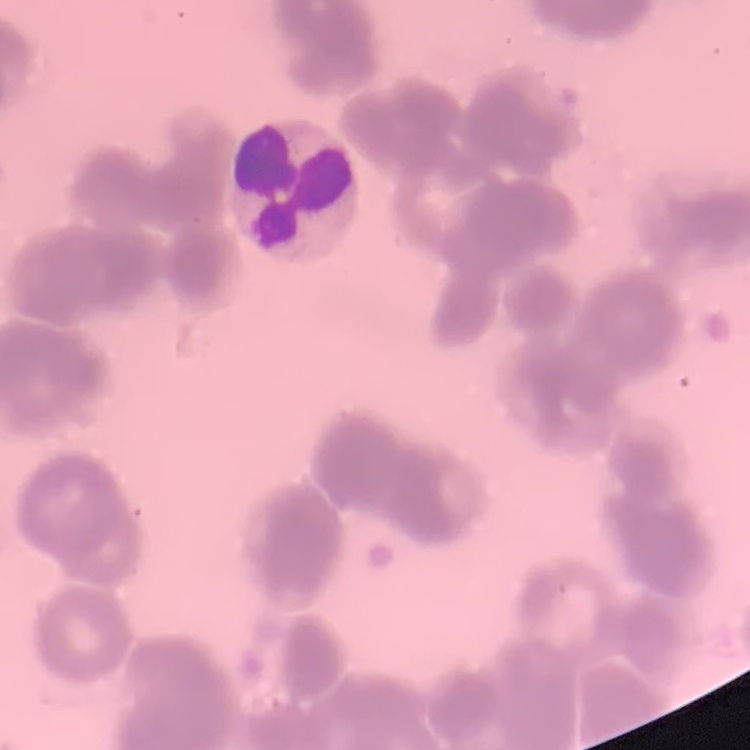
The red blood cells show rouleaux formation. Thin blood smear. Stained with either Field's or Giemsa. One tile cut from a larger photomicrograph.